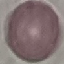

Malaria status: uninfected. Giemsa-stained preparation. Thin smear of blood. Photographed with a smartphone camera at the microscope eyepiece. Cell patch, automatically extracted from a larger field of view and resized to 64 × 64 pixels.